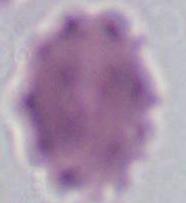 Captured at 1000x magnification. Photomicrograph. A red blood cell is shown.